State which parasite is depicted.
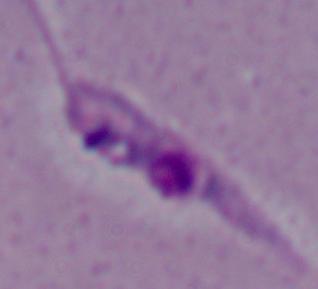
Leishmania.

Summary:
  - Modality: micrograph
  - Magnification: 1000x